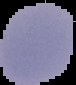
From a thin blood film. Image is 76×85 pixels. Malaria status: uninfected. Cell region segmented out of the field of view; the surrounding area is masked to black.